Report the malaria status of this cell.
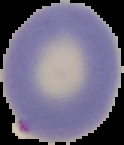
Parasitized.

Summary:
  - Image type: cell region segmented out of the field of view; surrounding area masked to black
  - Image size: 124×145 pixels
  - Preparation: thin blood smear